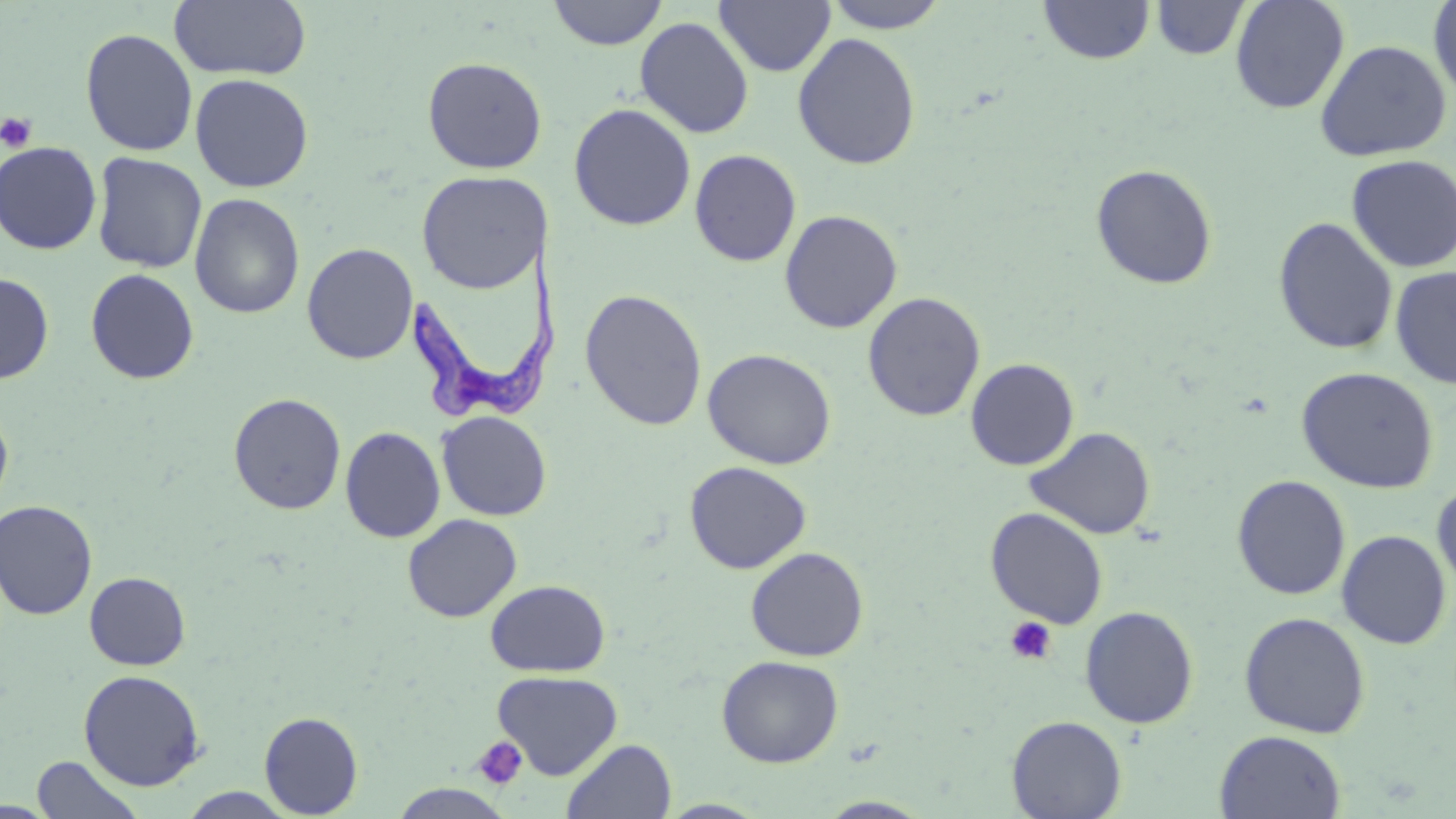 Approximate bounding boxes as [x1, y1, x2, y2] in pixels. Uninfected red blood cell locations: [169, 0, 313, 82], [547, 0, 667, 50], [713, 0, 836, 77], [821, 0, 952, 33], [1038, 0, 1155, 65], [1230, 0, 1349, 114], [1427, 0, 1456, 105], [1151, 1, 1250, 60], [634, 16, 754, 138], [80, 28, 198, 157], [792, 32, 921, 170], [1314, 39, 1452, 161], [422, 56, 548, 175], [190, 73, 314, 192], [568, 103, 697, 231], [0, 141, 102, 254], [689, 149, 801, 267], [91, 152, 208, 273], [1346, 153, 1456, 273], [1090, 163, 1218, 290], [416, 171, 549, 293], [189, 193, 305, 320], [780, 209, 903, 333], [1273, 216, 1398, 355], [301, 242, 418, 364], [1390, 265, 1456, 389], [85, 268, 199, 384], [0, 272, 54, 383], [579, 288, 708, 431], [862, 291, 985, 421], [702, 348, 837, 469], [965, 358, 1079, 470], [1296, 367, 1439, 493], [228, 392, 346, 515], [0, 404, 14, 514], [437, 411, 552, 521], [340, 426, 445, 542], [1025, 426, 1156, 539], [684, 461, 812, 574], [1231, 475, 1351, 599], [1431, 480, 1456, 597], [0, 499, 98, 620], [985, 507, 1109, 629], [403, 514, 522, 622], [1336, 529, 1452, 649], [745, 547, 869, 661], [84, 571, 191, 670], [486, 579, 610, 677], [1080, 606, 1199, 728], [1239, 611, 1371, 738], [716, 655, 843, 767], [78, 669, 206, 791], [492, 669, 623, 779], [259, 711, 363, 818], [1007, 715, 1127, 818], [1215, 730, 1346, 818], [561, 738, 677, 819], [30, 755, 146, 819], [390, 784, 514, 819], [177, 788, 298, 818], [816, 796, 935, 818], [658, 799, 772, 818]. Trypanosoma brucei locations: [400, 234, 565, 425]. Platelet locations: [0, 113, 38, 153], [1003, 616, 1058, 666], [472, 735, 529, 791]. Slide-level diagnosis: Trypanosoma brucei. 1000x magnification. May-Grünwald-Giemsa-stained preparation. Light microscopy. Single field of view. Thin blood smear. Image is 1456×819 pixels.